State which parasite is depicted.
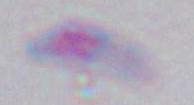
Toxoplasma gondii.

1000x magnification. Photomicrograph.